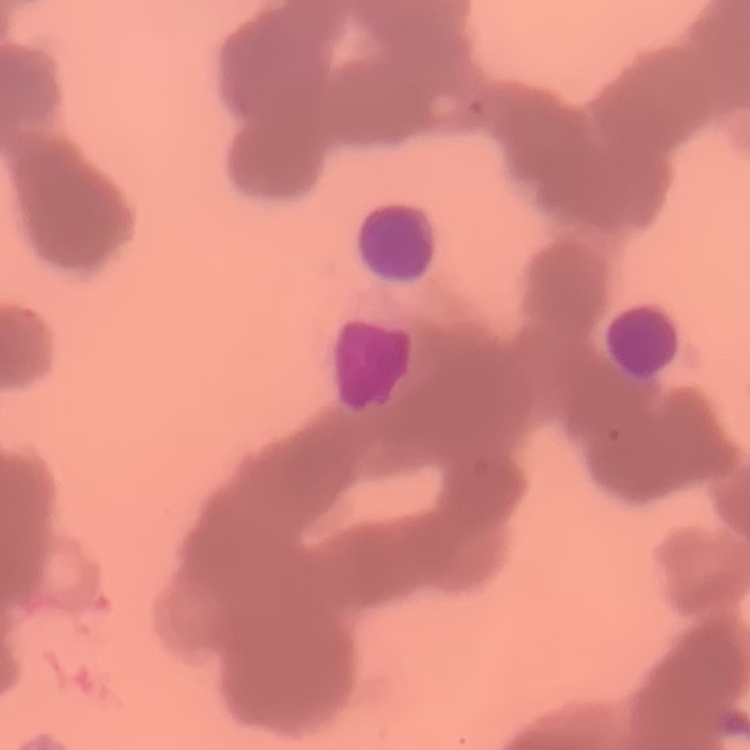
The red blood cells show rouleaux formation. Field's or Giemsa stain. One tile cut from a larger photomicrograph. Thin blood film.